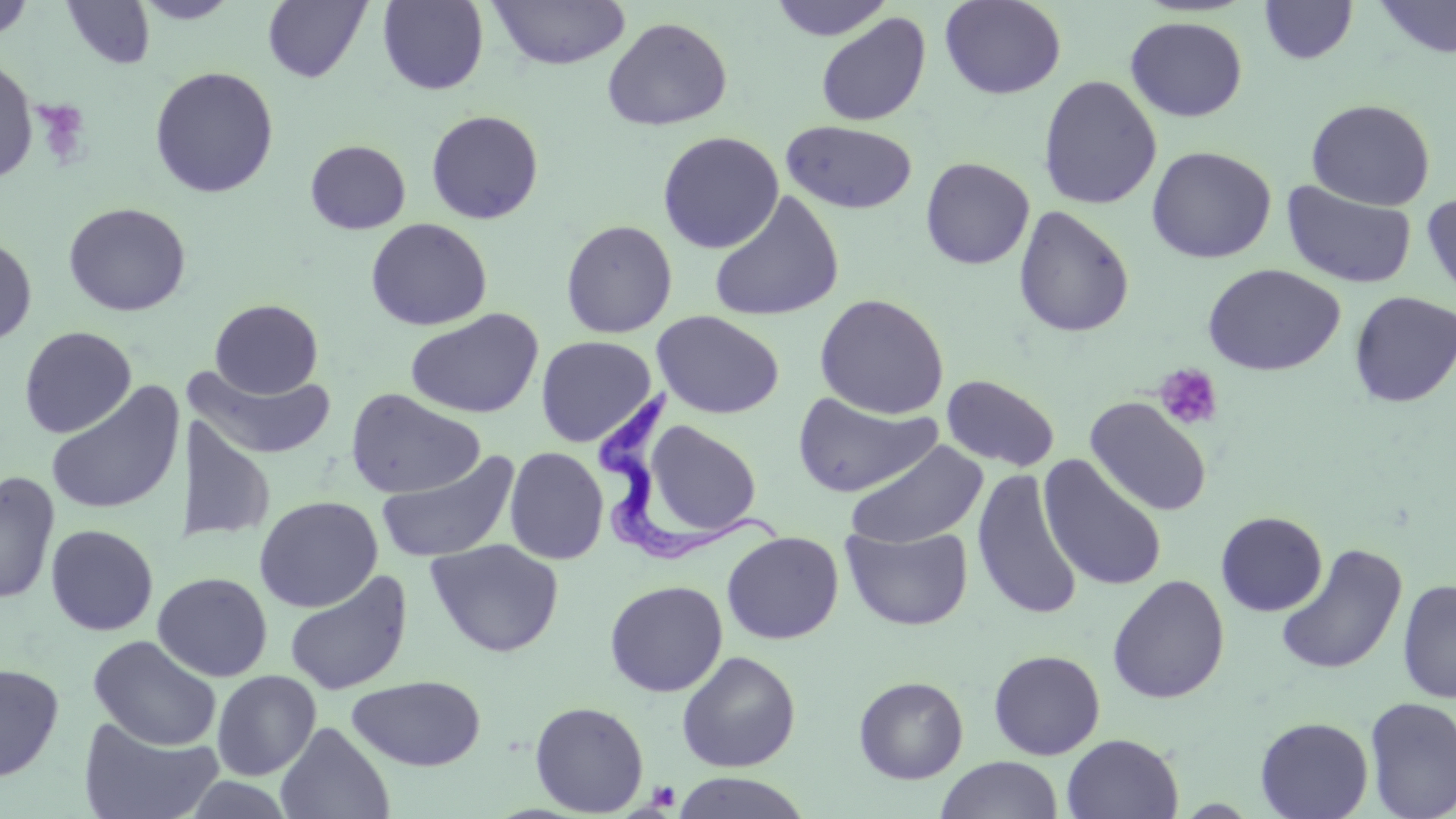
Summary:
  - Coordinate format: approximate bounding boxes as (x1, y1, x2, y2) in pixels
  - Uninfected red blood cell locations: (0, 0, 36, 42), (60, 0, 156, 69), (134, 0, 241, 24), (488, 0, 631, 70), (770, 0, 893, 41), (940, 0, 1066, 100), (1373, 0, 1456, 60), (262, 1, 371, 83), (377, 1, 489, 95), (1258, 1, 1358, 64), (815, 12, 931, 127), (1126, 16, 1247, 122), (601, 17, 733, 131), (0, 59, 38, 182), (149, 66, 279, 199), (1038, 75, 1162, 210), (1306, 98, 1435, 210), (425, 110, 544, 224), (781, 119, 918, 215), (658, 131, 784, 254), (305, 140, 411, 234), (1146, 145, 1276, 264), (920, 157, 1035, 269), (1281, 179, 1417, 289), (708, 191, 846, 323), (1421, 191, 1456, 309), (63, 202, 192, 317), (1012, 206, 1134, 338), (365, 218, 492, 331), (560, 219, 678, 339), (0, 236, 37, 346), (1202, 263, 1345, 376), (1349, 291, 1456, 408), (814, 293, 949, 419), (209, 299, 323, 398), (405, 308, 544, 419), (651, 310, 784, 419), (19, 326, 137, 438), (535, 335, 658, 447), (186, 364, 337, 460), (942, 374, 1060, 473), (44, 382, 186, 517), (345, 388, 486, 499), (791, 393, 943, 498), (1084, 397, 1212, 517), (186, 413, 275, 541), (639, 420, 764, 540), (845, 441, 988, 549), (504, 446, 608, 564), (375, 450, 521, 563), (1039, 455, 1167, 591), (971, 467, 1083, 621), (1, 470, 60, 606), (254, 495, 383, 613), (1215, 511, 1327, 616), (45, 524, 159, 636), (841, 524, 973, 631), (722, 531, 843, 645), (426, 538, 564, 657), (1274, 543, 1408, 676), (284, 570, 412, 696), (152, 572, 273, 682), (1107, 575, 1230, 705), (1397, 579, 1456, 705), (604, 580, 728, 697), (88, 634, 222, 751), (677, 650, 801, 772), (988, 650, 1105, 760), (0, 663, 64, 782), (212, 670, 321, 780), (347, 675, 486, 771), (854, 676, 968, 784), (1364, 696, 1456, 818), (529, 700, 649, 816), (1255, 716, 1374, 819), (78, 717, 223, 819), (275, 721, 395, 819), (1061, 733, 1184, 819), (936, 756, 1064, 819), (672, 772, 812, 818)
  - Platelet locations: (31, 99, 92, 169), (1155, 363, 1224, 431), (647, 780, 680, 811)
  - Trypanosoma brucei locations: (591, 384, 786, 564)
  - Slide-level diagnosis: Trypanosoma brucei
  - Preparation: thin blood smear
  - Stain: May-Grünwald-Giemsa
  - Image size: 1456×819 pixels
  - Modality: optical microscopy
  - Field of view: single
  - Magnification: 1000x